Identify the parasite.
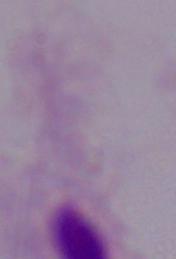

A trichomonad.

Micrograph. Captured at 1000x magnification.